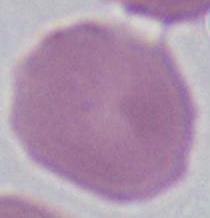
identification = erythrocyte
modality = micrograph
magnification = 1000x